Describe the morphology of the red blood cells.
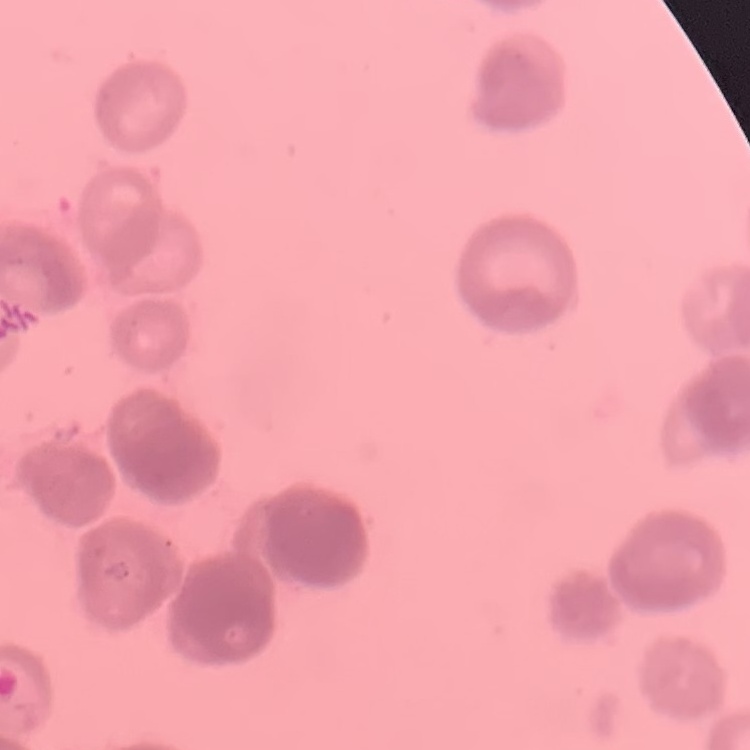
Rouleaux formation.

One tile cut from a larger photomicrograph. Thin peripheral smear. Field's or Giemsa stain.